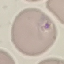
Summary:
  - Result: no malaria parasites seen
  - Capture: smartphone through the microscope eyepiece
  - Preparation: thin blood film
  - Stain: Giemsa
  - Image type: cell patch, automatically extracted from a larger field of view and resized to 64 × 64 pixels